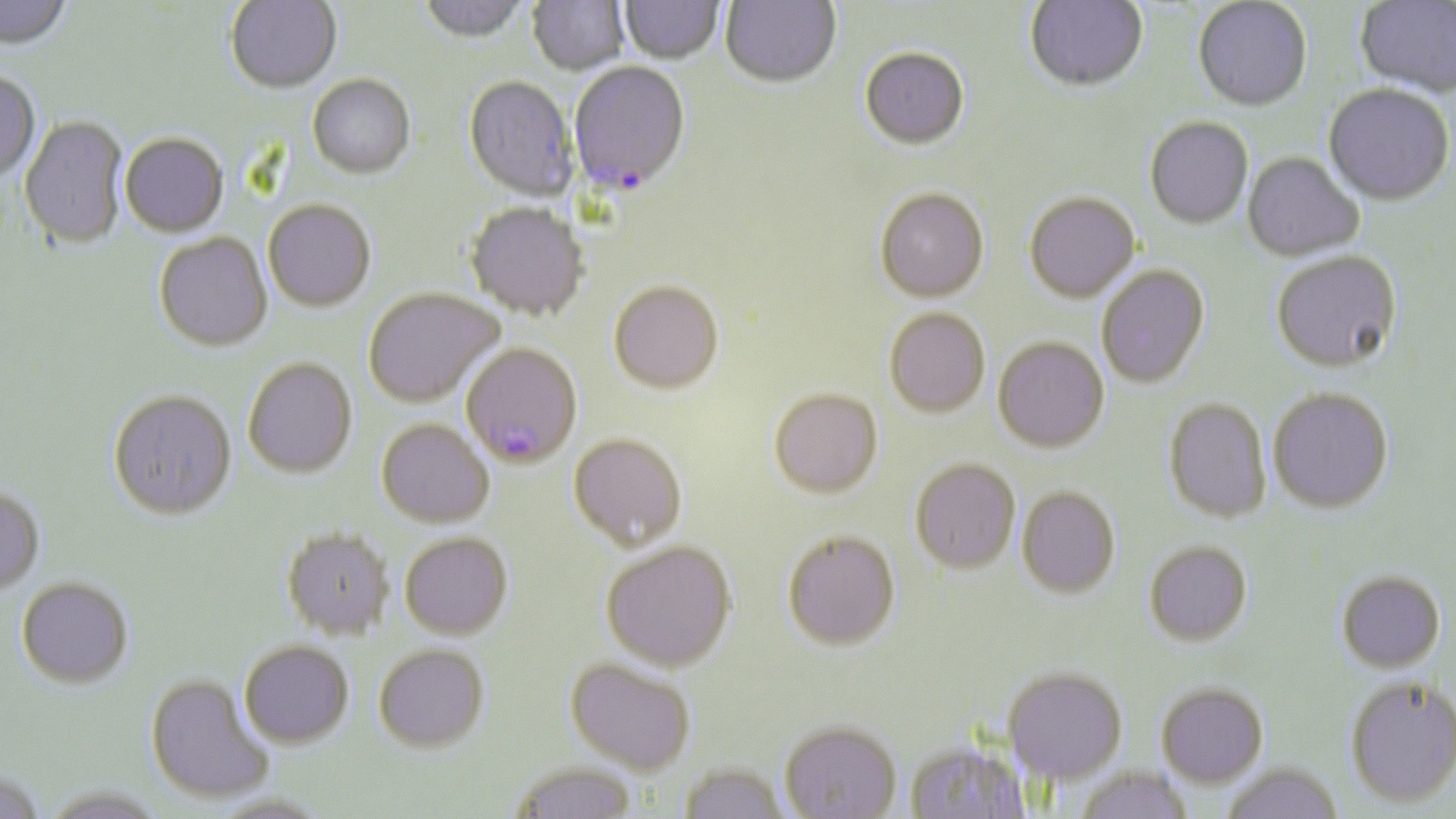

Summary:
  - Coordinate format: approximate bounding boxes as named x1/y1/x2/y2 corners in pixels
  - Uninfected red blood cell locations: (x1=0, y1=0, x2=74, y2=51), (x1=225, y1=0, x2=342, y2=94), (x1=415, y1=0, x2=532, y2=45), (x1=527, y1=0, x2=629, y2=77), (x1=1025, y1=0, x2=1148, y2=91), (x1=1192, y1=0, x2=1312, y2=111), (x1=619, y1=1, x2=724, y2=66), (x1=720, y1=1, x2=842, y2=89), (x1=1355, y1=1, x2=1456, y2=97), (x1=859, y1=47, x2=970, y2=150), (x1=0, y1=70, x2=41, y2=182), (x1=307, y1=75, x2=415, y2=180), (x1=462, y1=77, x2=577, y2=202), (x1=1324, y1=83, x2=1455, y2=206), (x1=19, y1=115, x2=128, y2=249), (x1=1144, y1=116, x2=1253, y2=228), (x1=120, y1=133, x2=228, y2=237), (x1=1243, y1=151, x2=1365, y2=261), (x1=875, y1=187, x2=989, y2=301), (x1=1024, y1=191, x2=1140, y2=302), (x1=263, y1=199, x2=376, y2=311), (x1=465, y1=202, x2=589, y2=321), (x1=154, y1=232, x2=272, y2=352), (x1=1270, y1=249, x2=1402, y2=372), (x1=1096, y1=264, x2=1209, y2=388), (x1=608, y1=279, x2=724, y2=393), (x1=363, y1=286, x2=503, y2=407), (x1=884, y1=307, x2=990, y2=417), (x1=993, y1=337, x2=1109, y2=452), (x1=242, y1=356, x2=358, y2=477), (x1=769, y1=387, x2=882, y2=498), (x1=1267, y1=387, x2=1394, y2=513), (x1=108, y1=389, x2=237, y2=519), (x1=1163, y1=397, x2=1273, y2=523), (x1=376, y1=418, x2=494, y2=527), (x1=568, y1=433, x2=687, y2=550), (x1=910, y1=457, x2=1021, y2=574), (x1=0, y1=486, x2=45, y2=593), (x1=1017, y1=486, x2=1120, y2=597), (x1=280, y1=527, x2=395, y2=640), (x1=782, y1=530, x2=900, y2=651), (x1=399, y1=531, x2=513, y2=640), (x1=600, y1=540, x2=737, y2=671), (x1=1144, y1=541, x2=1253, y2=646), (x1=1336, y1=570, x2=1446, y2=672), (x1=16, y1=577, x2=134, y2=689), (x1=239, y1=641, x2=355, y2=748), (x1=373, y1=643, x2=490, y2=753), (x1=565, y1=658, x2=697, y2=775), (x1=1002, y1=666, x2=1128, y2=785), (x1=145, y1=674, x2=273, y2=804), (x1=1344, y1=675, x2=1456, y2=808), (x1=1155, y1=682, x2=1268, y2=788), (x1=779, y1=720, x2=902, y2=818), (x1=904, y1=739, x2=1032, y2=818), (x1=509, y1=761, x2=639, y2=819), (x1=677, y1=762, x2=792, y2=818), (x1=1220, y1=762, x2=1343, y2=819), (x1=1074, y1=766, x2=1194, y2=819), (x1=0, y1=769, x2=47, y2=819), (x1=39, y1=785, x2=170, y2=819), (x1=207, y1=794, x2=336, y2=819)
  - Plasmodium falciparum-infected red blood cell locations: (x1=568, y1=63, x2=691, y2=196), (x1=461, y1=341, x2=583, y2=468)
  - Slide-level diagnosis: Plasmodium falciparum
  - Image size: 1456×819 pixels
  - Stain: May-Grünwald-Giemsa
  - Magnification: 1000x
  - Field of view: single
  - Preparation: thin blood smear
  - Modality: light microscopy